Report the malaria status of this cell.
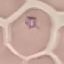
It is parasitized.

Summary:
  - Stain: Giemsa
  - Image type: cell patch, automatically extracted from a larger field of view and resized to 64 × 64 pixels
  - Capture: smartphone camera at the microscope eyepiece
  - Preparation: thin blood smear